State which parasite is depicted.
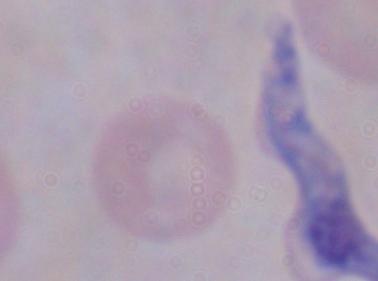

A trypanosome.

Summary:
  - Magnification: 1000x
  - Modality: micrograph